State which parasite is depicted.
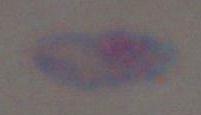

Toxoplasma gondii.

Summary:
  - Modality: photomicrograph
  - Magnification: 1000x